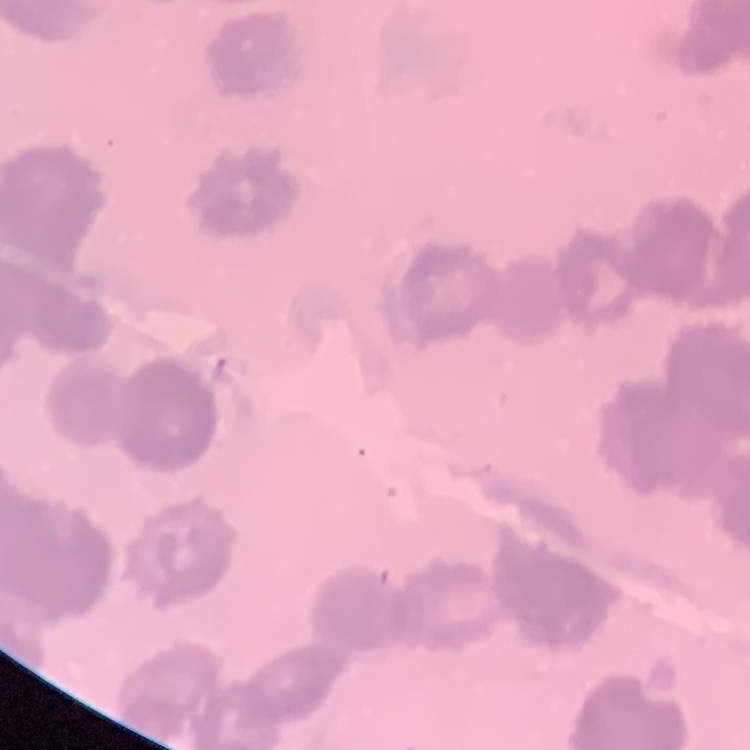

The red blood cells exhibit rouleaux formation. Field's or Giemsa stain. Thin blood film. One tile cut from a larger photomicrograph.